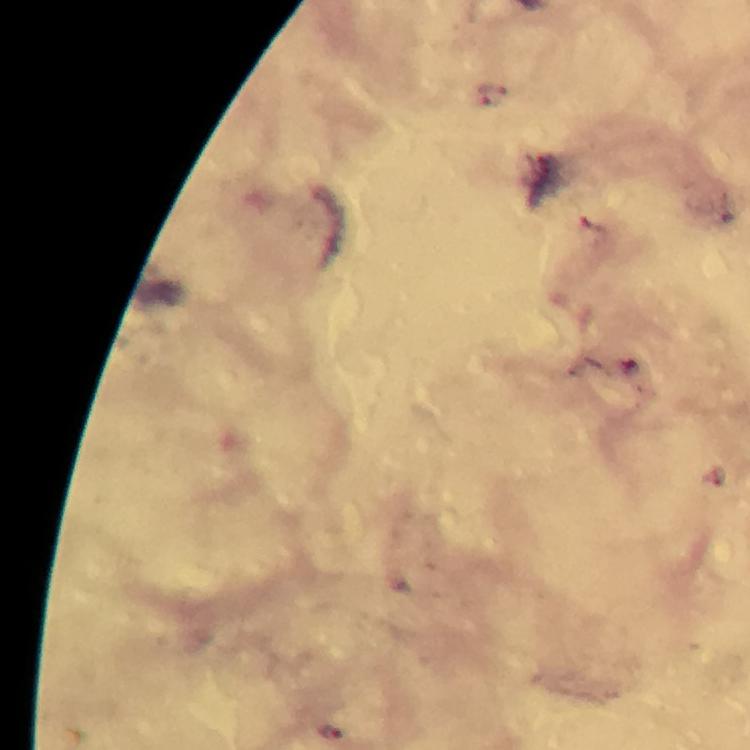
Approximate centers as [x, y] in pixels. Plasmodium parasite locations: [491, 94], [333, 732]. Immersion oil was used. A crop from one field of view. Giemsa stain. Photographed with a smartphone mounted on the microscope. Thick smear. From a diagnostic examination for malaria. Image is 750×750 pixels. At 100x magnification.